Give the location of every parasitized red blood cell.
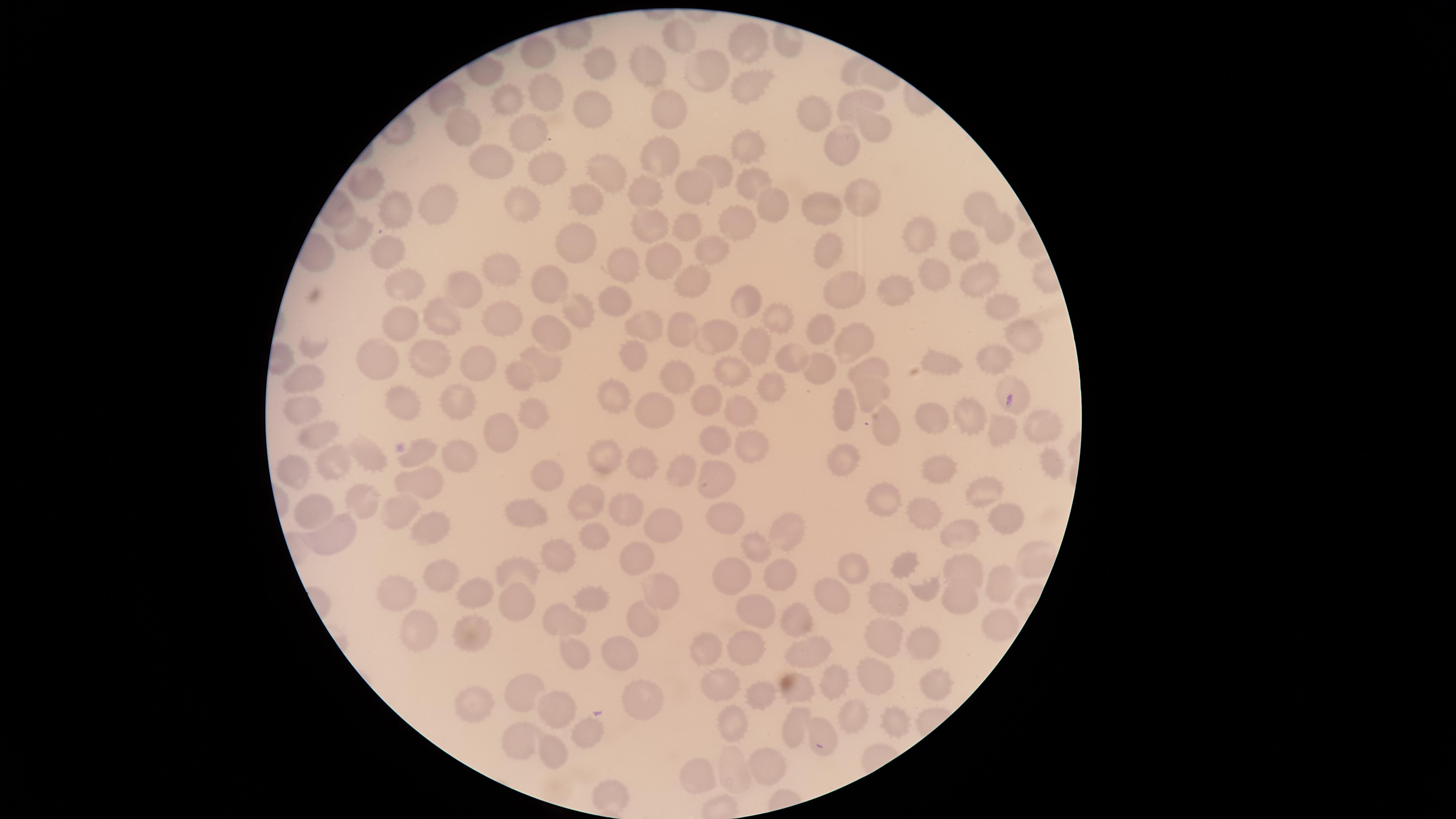
Approximate marker points as (x, y) in pixels.
Parasitized red blood cells: (1009, 400).

Approximate marker points as (x, y) in pixels. Uninfected red blood cells: (685, 39), (748, 45), (541, 53), (596, 60), (642, 67), (699, 71), (749, 89), (541, 91), (863, 98), (509, 99), (590, 111), (660, 111), (810, 114), (469, 129), (871, 130), (528, 133), (837, 145), (746, 146), (492, 160), (664, 162), (542, 164), (718, 173), (606, 177), (754, 180), (368, 187), (699, 192), (650, 198), (859, 200), (585, 204), (977, 204), (772, 205), (442, 206), (525, 207), (400, 212), (830, 212), (650, 226), (995, 226), (736, 227), (920, 232), (694, 233), (350, 235), (715, 245), (585, 249), (967, 249), (390, 254), (830, 254), (662, 262), (624, 263), (503, 270), (978, 274), (932, 276), (554, 281), (400, 282), (460, 284), (843, 284), (696, 288), (899, 293), (755, 302), (612, 303), (1000, 311), (578, 316), (439, 317), (773, 320), (501, 323), (402, 324), (823, 325), (645, 326), (681, 332), (1024, 333), (719, 335), (549, 339), (849, 342), (761, 349), (379, 357), (631, 359), (786, 360), (427, 361), (1000, 361), (479, 365), (942, 365), (550, 368), (868, 369), (821, 371), (733, 372), (523, 375), (301, 377), (682, 378), (779, 386), (870, 393), (402, 395), (458, 398), (613, 399), (709, 400), (305, 408), (846, 409), (733, 412), (535, 416), (652, 416), (932, 417), (973, 417), (1039, 422), (884, 428), (495, 429), (1006, 430), (322, 432), (754, 440), (708, 441), (420, 451), (463, 452), (364, 455), (606, 460), (339, 464), (844, 464), (646, 465), (1052, 468), (682, 470), (941, 470), (293, 473), (552, 473), (716, 478), (420, 485), (983, 493), (887, 500), (362, 502), (310, 503), (582, 505), (630, 508), (400, 509), (923, 511), (521, 515), (1002, 517), (722, 518), (422, 525), (665, 525), (959, 530), (327, 536), (786, 537), (593, 542), (755, 550), (563, 559), (640, 562), (905, 566), (966, 568), (855, 569), (515, 570), (441, 574), (735, 579), (1001, 579), (775, 580), (658, 590), (921, 592), (832, 593), (406, 597), (470, 598), (883, 601), (516, 602), (959, 602), (596, 603), (753, 614), (567, 619), (643, 623), (799, 623), (1003, 624), (422, 626), (471, 630), (878, 641), (923, 646), (745, 647), (576, 648), (807, 653), (706, 654), (615, 666), (876, 677), (828, 682), (723, 684), (935, 685), (796, 687), (527, 688), (756, 690), (475, 704), (643, 707), (556, 708), (854, 713), (892, 721), (730, 723), (794, 732), (591, 733), (527, 735), (827, 737), (556, 748), (762, 766), (733, 770), (703, 780), (617, 794). Image is 1456×819 pixels. Thin blood film. One field of view of the specimen. Photographed with a smartphone camera through the microscope eyepiece. The visible region is circular. Giemsa stain. Species: Plasmodium falciparum.